Assess this cell for malaria.
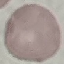

It is uninfected.

Summary:
  - Preparation: thin blood smear
  - Stain: Giemsa
  - Image type: cell patch, automatically extracted from a larger field of view and resized to 64 × 64 pixels
  - Capture: smartphone camera at the microscope eyepiece